Name the cell type shown.
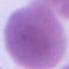

An erythrocyte.

Photomicrograph. 1000x magnification.